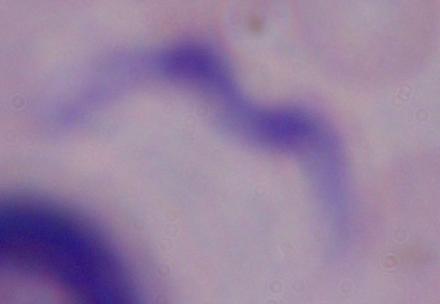

Summary:
  - Identification: trypanosome
  - Magnification: 1000x
  - Modality: micrograph